Report the malaria status of this cell.
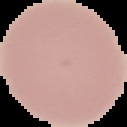
Uninfected.

Cell region segmented out of the field of view; the surrounding area is masked to black. Image is 127×127 pixels. From a thin blood film.